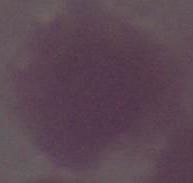
A red blood cell is shown. Micrograph. Captured at 1000x magnification.